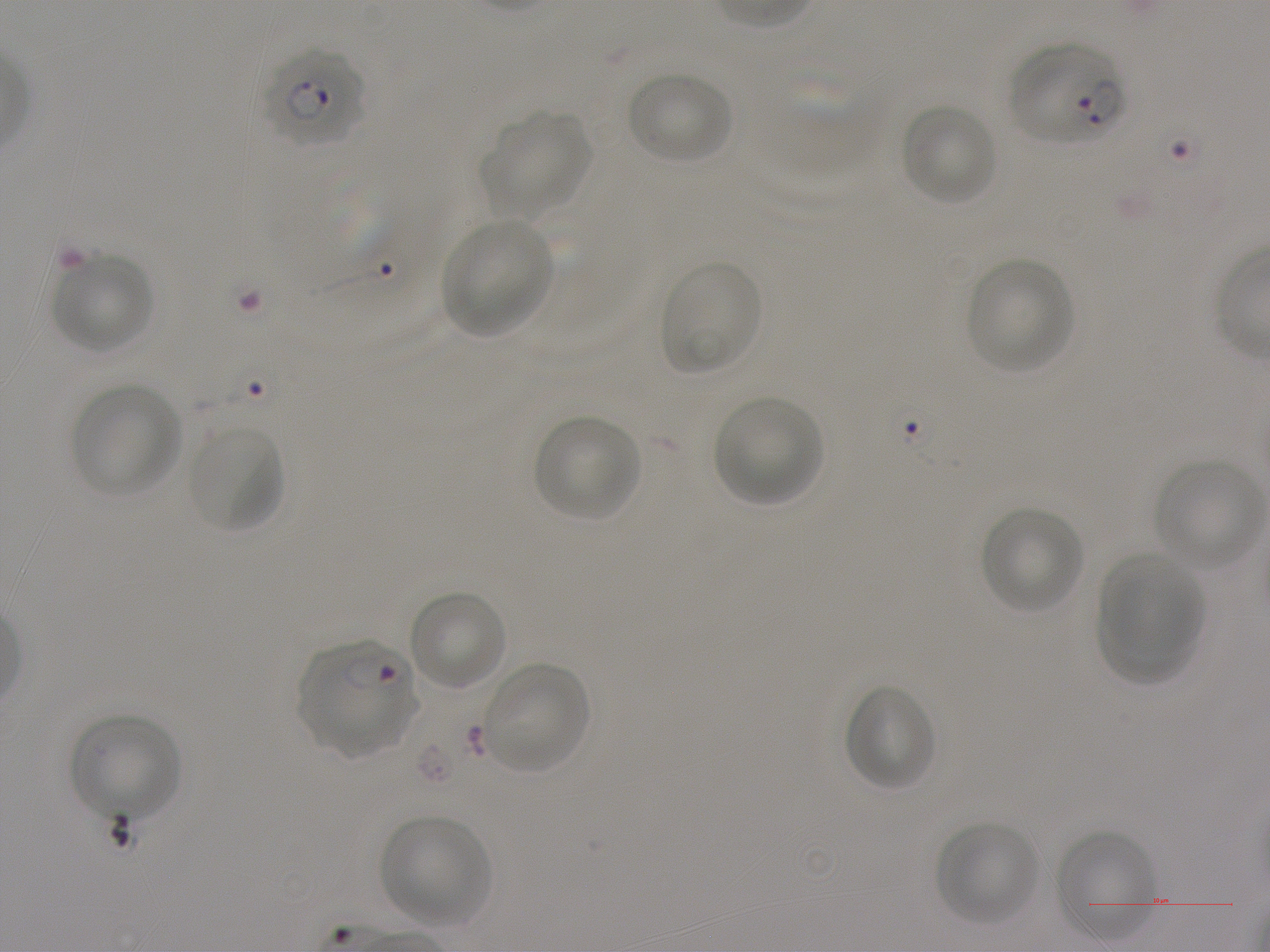 Approximate bounding boxes as (x1, y1, x2, y2) in pixels. Not every red blood cell is marked. A life-cycle stage — or a range of stages, where the recorded stages span more than one — follows each staged infected red blood cell. Locations of red blood cells of indeterminate infection status: (292, 168, 416, 293). Locations of uninfected red blood cells: (754, 60, 878, 185), (627, 71, 733, 166), (900, 103, 998, 207), (481, 112, 591, 215), (443, 218, 554, 335), (51, 253, 154, 354), (964, 258, 1074, 373), (659, 259, 764, 376), (71, 383, 182, 497), (712, 396, 823, 505), (535, 414, 640, 522), (188, 424, 286, 535), (1153, 458, 1264, 569), (981, 506, 1083, 613), (1098, 554, 1204, 663), (408, 589, 507, 692), (1097, 601, 1191, 684), (481, 662, 589, 773), (843, 684, 937, 791), (70, 714, 182, 822), (382, 815, 491, 926), (936, 821, 1039, 926), (1053, 830, 1156, 938). Locations of infected red blood cells: (1008, 41, 1128, 146) ring; (259, 45, 366, 146) ring; (297, 639, 418, 757) ring. Oil immersion, 100x objective (numerical aperture 1.25). Single field of view. Image is 1270×952 pixels. Blood group of the donor: A+. Thin blood film. Static in-vitro culture of P. falciparum strain NF54. Giemsa-stained preparation.